Outline each blood parasite and name the species.
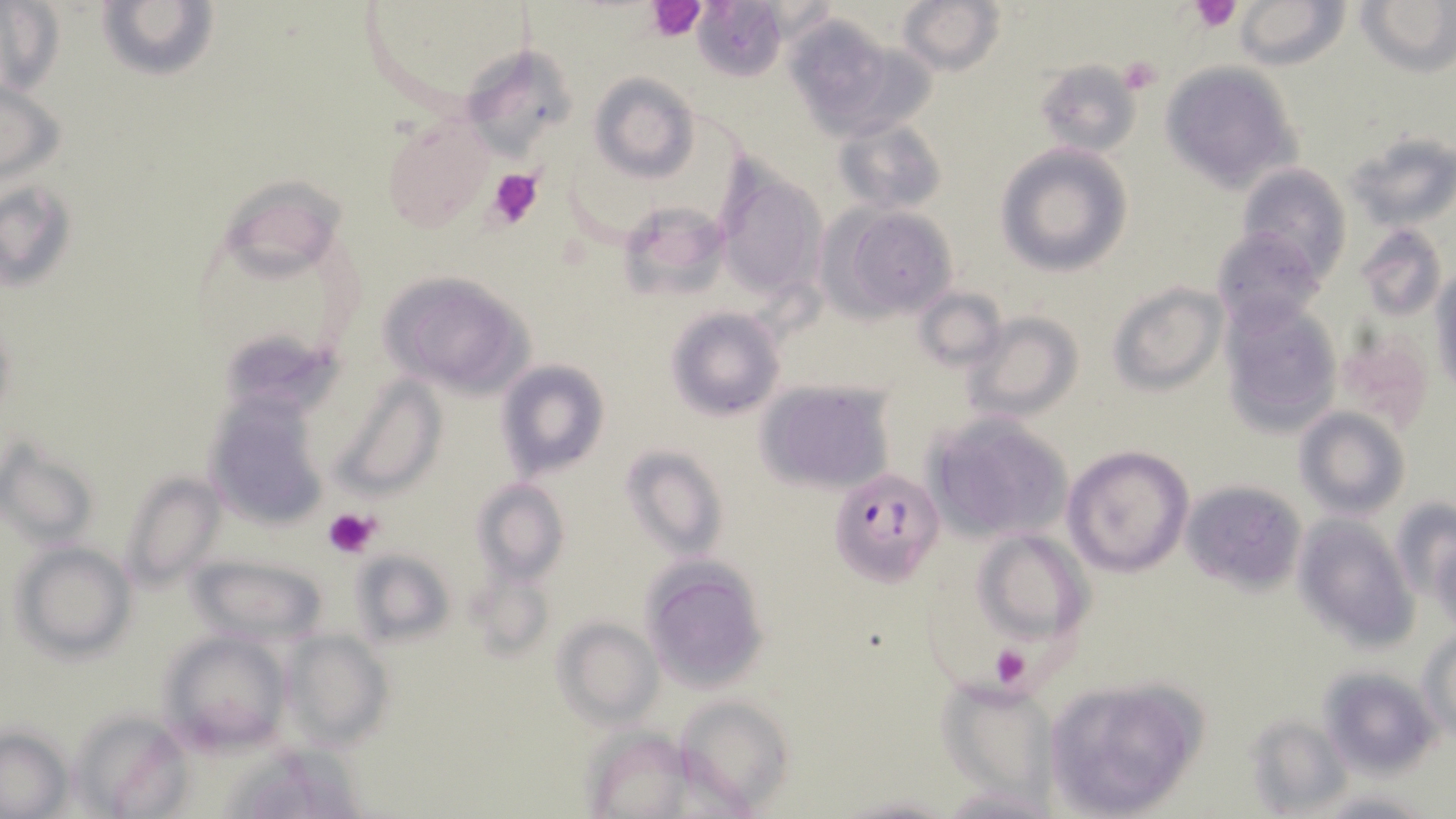

Approximate bounding boxes as (x1,y1)-(x2,y2) corner pairs in pixels.
Plasmodium falciparum-infected red blood cells: (829,468)-(943,584).
No Plasmodium ovale, Plasmodium malariae, Plasmodium vivax, Babesia divergens, or Trypanosoma brucei observed.

Uninfected red blood cell locations: (690,0)-(790,83), (898,0)-(1005,77), (1233,0)-(1351,70), (1359,0)-(1454,75), (97,1)-(218,83), (0,3)-(64,96), (784,19)-(928,137), (480,50)-(574,155), (1031,60)-(1140,157), (1159,63)-(1301,193), (590,73)-(698,183), (0,76)-(65,190), (382,117)-(492,235), (835,119)-(947,217), (1346,132)-(1455,233), (995,143)-(1134,277), (716,162)-(830,304), (1237,164)-(1351,281), (225,173)-(354,269), (3,177)-(78,294), (621,202)-(744,298), (830,206)-(959,323), (1356,223)-(1447,322), (1210,225)-(1323,330), (1430,269)-(1455,396), (380,271)-(535,395), (1106,282)-(1228,395), (914,286)-(1008,373), (1219,298)-(1344,435), (665,307)-(786,422), (965,311)-(1085,422), (228,326)-(355,412), (1333,328)-(1435,434), (498,359)-(609,479), (336,374)-(445,496), (758,379)-(896,494), (205,396)-(325,530), (1296,407)-(1409,518), (925,412)-(1074,545), (1,439)-(97,549), (621,444)-(727,560), (1062,444)-(1193,578), (119,469)-(223,591), (471,476)-(569,586), (1182,479)-(1307,594), (1393,499)-(1453,609), (1293,514)-(1416,646), (969,529)-(1090,647), (1429,531)-(1456,633), (11,541)-(136,658), (350,547)-(456,647), (186,552)-(331,642), (642,557)-(769,691), (464,564)-(554,664), (554,618)-(662,726), (1421,629)-(1455,741), (159,631)-(295,752), (284,631)-(390,751), (1316,668)-(1439,775), (1040,675)-(1208,817), (938,679)-(1061,801), (677,695)-(794,811), (73,707)-(190,817), (1245,714)-(1352,814), (1,726)-(71,816), (580,727)-(696,817), (224,733)-(363,816), (935,782)-(1063,816), (1317,789)-(1434,817), (837,793)-(958,818). Platelet locations: (1189,0)-(1244,33), (643,1)-(709,41), (1118,57)-(1164,94), (486,167)-(545,230), (322,507)-(380,559), (989,645)-(1031,690). Slide-level diagnosis: Plasmodium falciparum. Captured at 1000x magnification. Thin blood smear. Optical microscopy. Image is 1456×819 pixels. May-Grünwald-Giemsa-stained preparation. One field of a larger specimen.